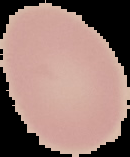
Summary:
  - Result: negative for Plasmodium parasites
  - Preparation: thin blood smear
  - Image size: 130×157 pixels
  - Image type: cell region segmented out of the field of view; surrounding area masked to black